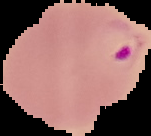
Malaria status: parasitized. From a thin blood film. Image is 151×136 pixels. Segmented cell region on a black background.